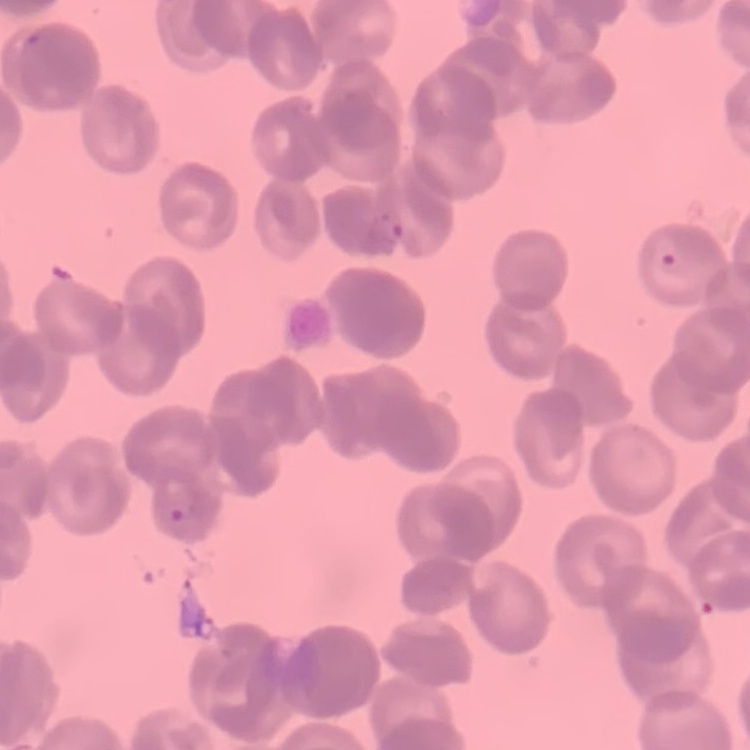

Summary:
  - Red blood cell morphology: rouleaux formation
  - Image type: one tile cut from a larger photomicrograph
  - Preparation: thin blood smear
  - Stain: Field's or Giemsa